Locate every leukocyte (white blood cell).
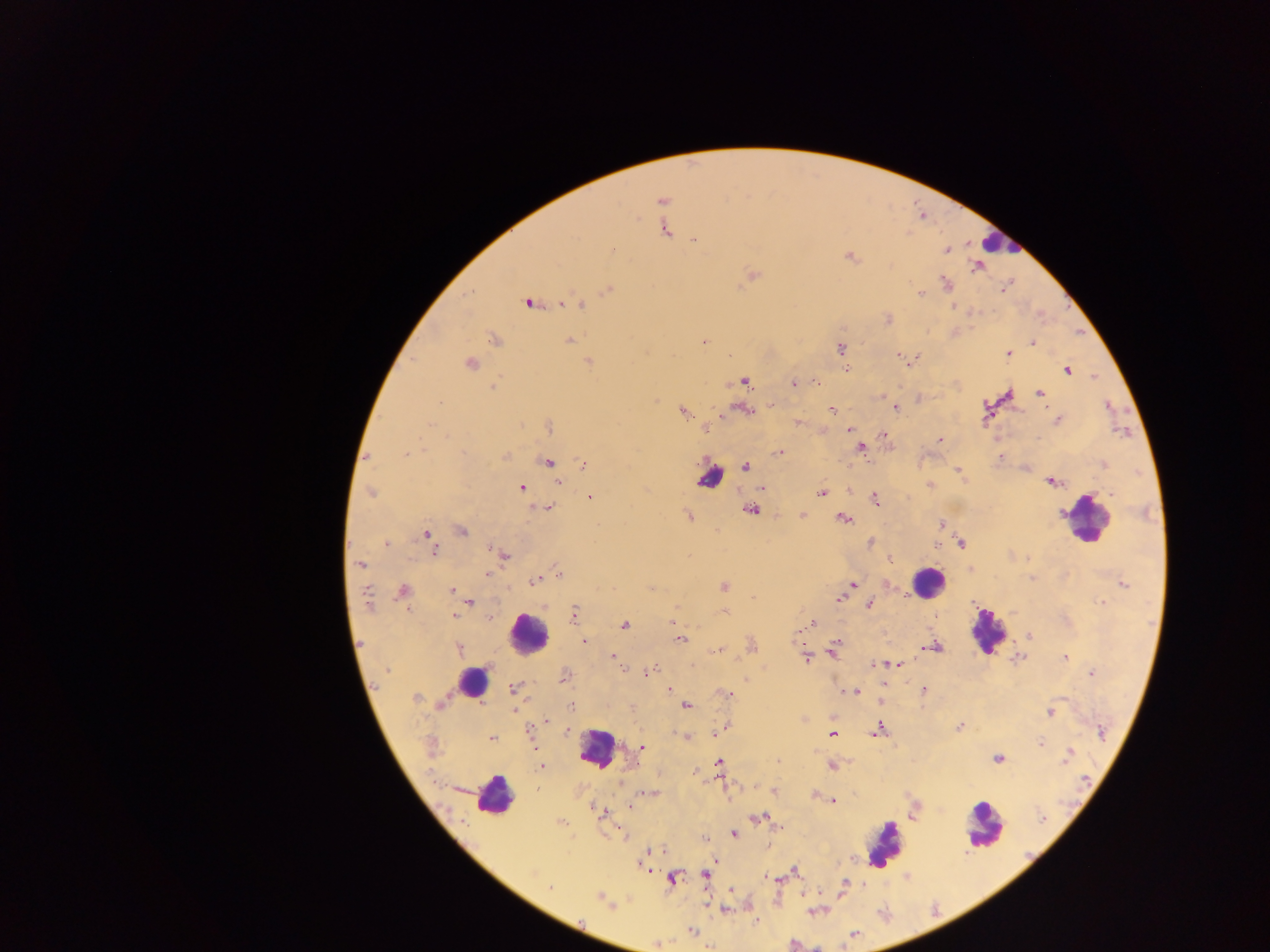

Approximate centers as {x, y} in pixels.
Leukocytes: {998, 241}, {709, 477}, {1088, 518}, {927, 583}, {987, 632}, {526, 634}, {471, 683}, {598, 749}, {492, 795}, {983, 824}, {886, 845}.

Summary:
  - Malaria parasite locations: {661, 200}, {665, 230}, {695, 240}, {613, 248}, {946, 250}, {850, 256}, {977, 268}, {751, 276}, {947, 284}, {1004, 288}, {608, 290}, {920, 294}, {527, 303}, {563, 303}, {579, 305}, {887, 320}, {495, 339}, {569, 340}, {704, 341}, {1033, 343}, {840, 348}, {1009, 354}, {900, 355}, {589, 362}, {470, 364}, {846, 368}, {1067, 370}, {744, 381}, {817, 382}, {794, 384}, {493, 388}, {1009, 393}, {1039, 393}, {881, 396}, {772, 405}, {896, 408}, {832, 409}, {745, 410}, {683, 412}, {1058, 420}, {798, 422}, {549, 427}, {849, 429}, {884, 434}, {940, 439}, {861, 449}, {779, 452}, {407, 454}, {505, 457}, {547, 462}, {583, 463}, {745, 467}, {958, 470}, {1053, 481}, {558, 482}, {930, 485}, {521, 487}, {762, 489}, {370, 493}, {822, 493}, {1112, 494}, {590, 498}, {874, 499}, {547, 508}, {750, 510}, {689, 516}, {802, 516}, {843, 518}, {942, 525}, {462, 531}, {427, 534}, {386, 544}, {962, 544}, {937, 545}, {435, 550}, {505, 555}, {890, 559}, {360, 565}, {487, 574}, {558, 574}, {535, 581}, {852, 585}, {1124, 585}, {724, 586}, {452, 590}, {403, 591}, {366, 596}, {753, 597}, {840, 599}, {469, 601}, {1102, 603}, {870, 604}, {724, 611}, {574, 613}, {455, 617}, {673, 622}, {811, 623}, {624, 625}, {1030, 636}, {681, 640}, {584, 643}, {836, 644}, {935, 647}, {459, 648}, {925, 648}, {718, 650}, {833, 650}, {612, 656}, {1065, 657}, {1017, 658}, {805, 659}, {873, 664}, {898, 664}, {623, 670}, {388, 671}, {650, 672}, {1092, 673}, {564, 677}, {745, 680}, {884, 684}, {513, 689}, {668, 690}, {923, 690}, {856, 692}, {726, 694}, {416, 698}, {880, 700}, {442, 704}, {571, 706}, {686, 706}, {513, 710}, {1050, 713}, {546, 720}, {725, 726}, {959, 727}, {567, 730}, {878, 730}, {716, 733}, {1102, 733}, {530, 734}, {832, 734}, {685, 736}, {492, 739}, {1041, 744}, {642, 748}, {1067, 756}, {997, 758}, {719, 762}, {831, 766}, {541, 767}, {775, 791}, {647, 792}, {815, 795}, {833, 801}, {631, 806}, {602, 814}, {757, 817}, {1043, 818}, {562, 823}, {621, 832}, {733, 834}, {706, 838}, {651, 851}, {794, 870}, {706, 874}, {672, 879}, {769, 879}, {844, 884}, {550, 888}, {599, 897}, {725, 909}, {692, 931}, {853, 935}
  - Field of view: single
  - Preparation: thick blood smear
  - Country: Ghana
  - Image size: 1270×952 pixels
  - Capture: mobile-phone photograph through a microscope